Look for Plasmodium parasites.
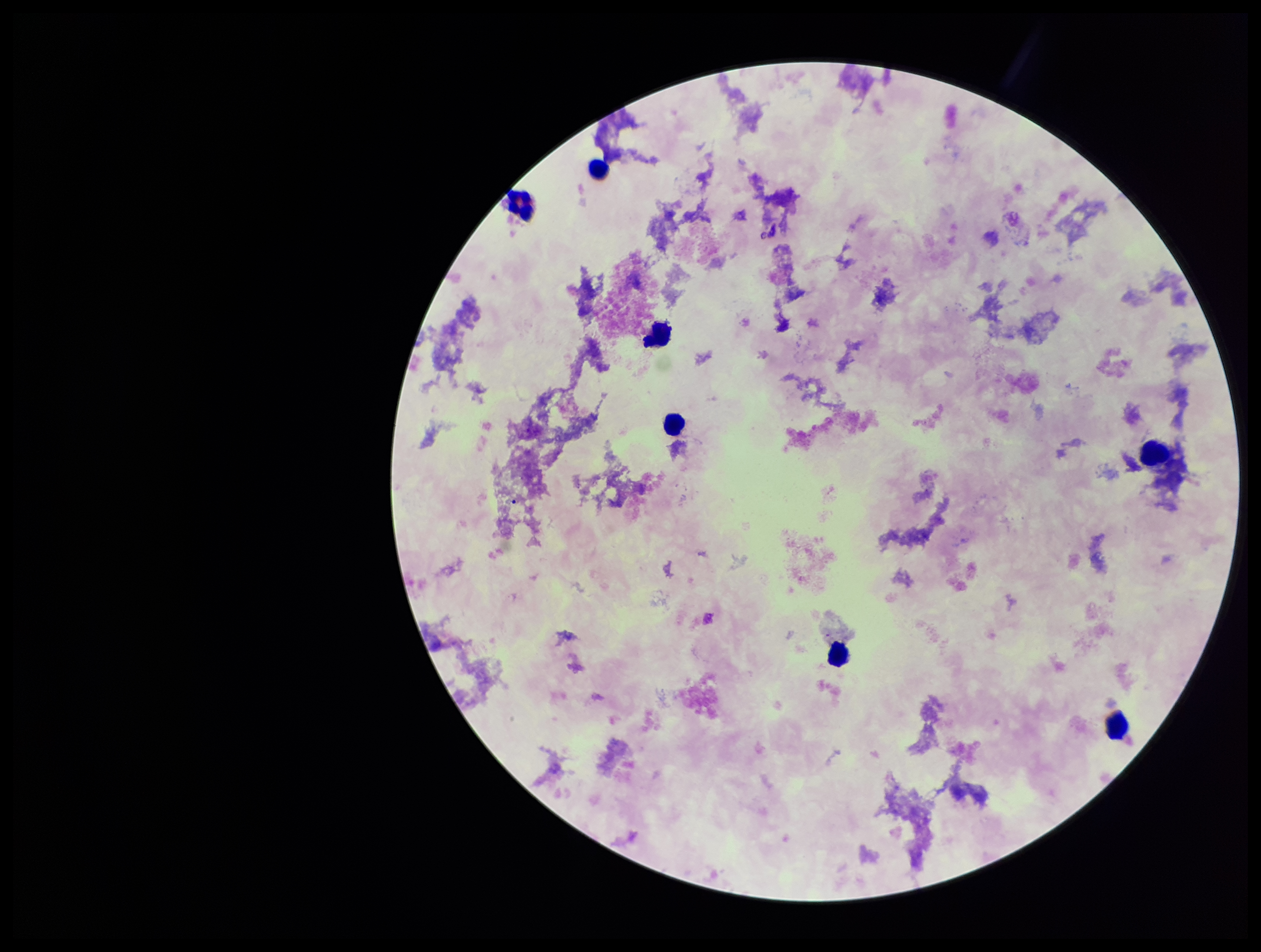

None seen.

Leukocyte count: 7. Patient malaria status: negative. Giemsa stain. Preparation: thick smear. One field from this slide. Smartphone photograph taken through the eyepiece of a microscope. Image is 1261×952 pixels. Parasite count: 0.